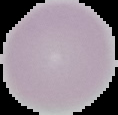

image size = 118×115 pixels
preparation = thin blood smear
result = no Plasmodium parasites detected
image type = segmented cell region with the area outside set to black